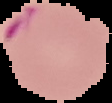
The area outside the segmented cell region is set to black. Malaria status: parasitized. From a thin blood film. Image is 112×103 pixels.